Identify the parasite.
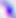

Toxoplasma gondii.

Micrograph. Captured at 400x magnification.